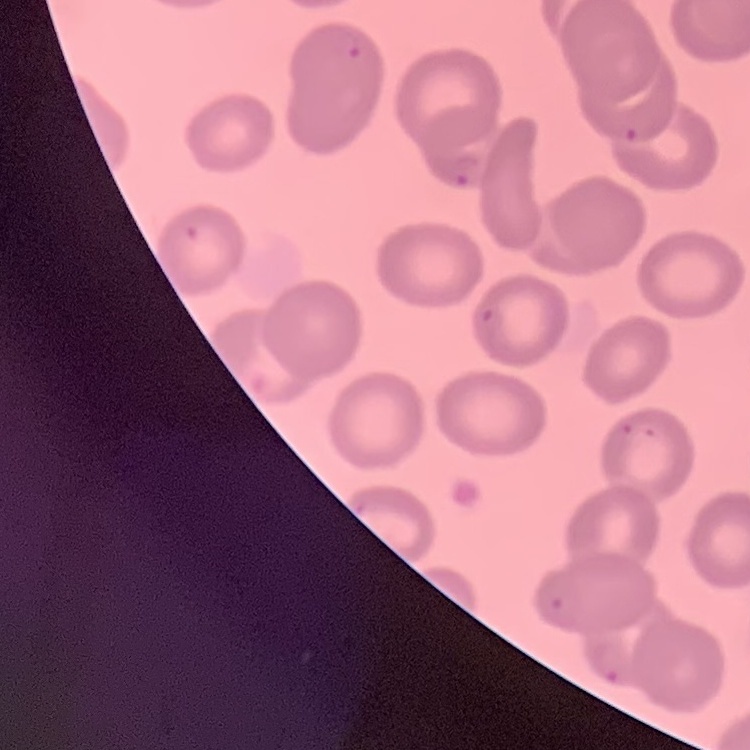
The erythrocytes show no rouleaux formation. One tile cut from a larger photomicrograph. Thin blood smear. Stained with either Field's or Giemsa.